Outline platelets.
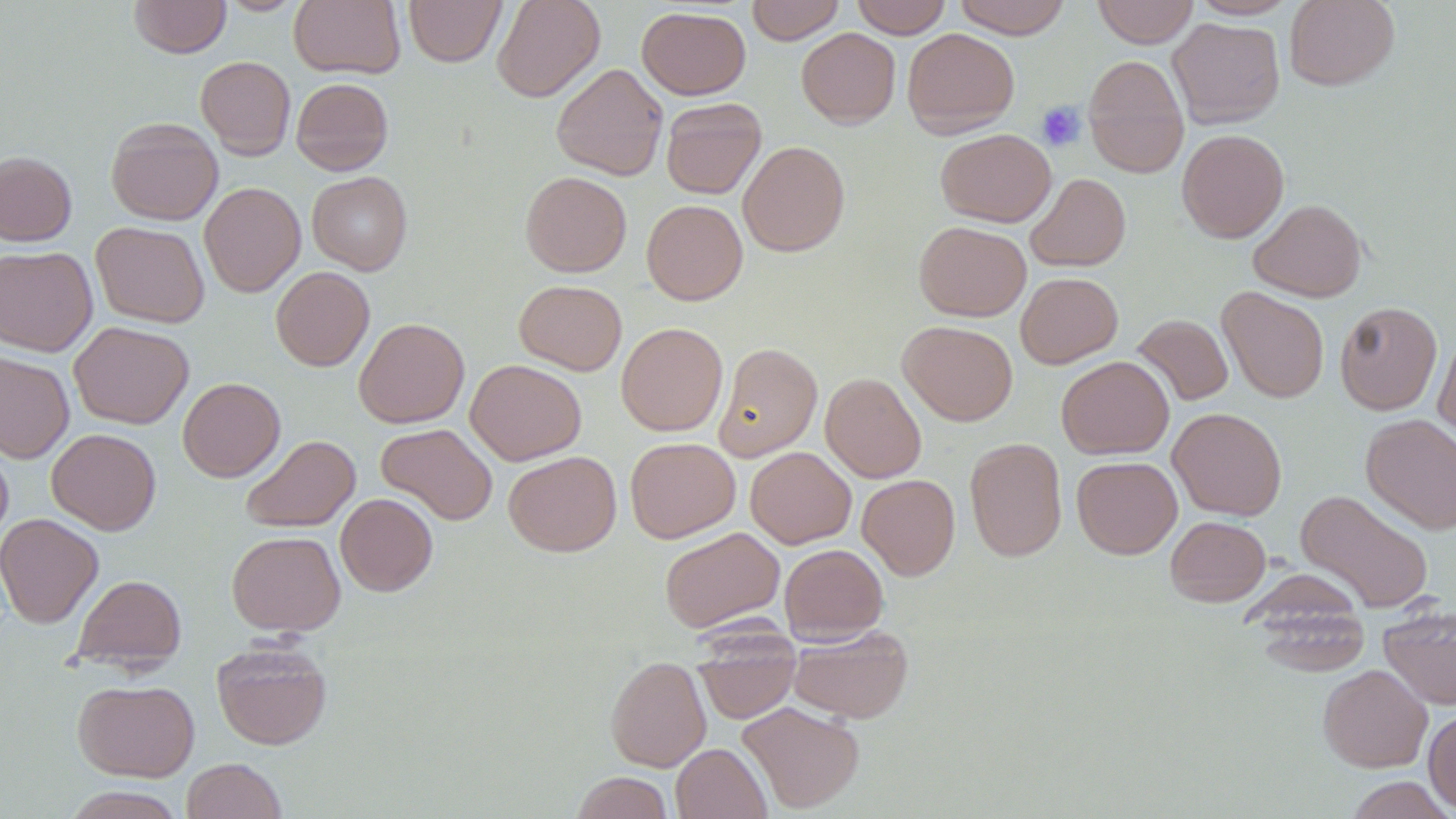
Approximate bounding boxes as named x1/y1/x2/y2 corners in pixels.
Platelets: (x1=1036, y1=101, x2=1086, y2=152).

slide-level diagnosis = no evidence of blood parasites
uninfected red blood cell locations = approximate bounding boxes as named x1/y1/x2/y2 corners in pixels: (x1=129, y1=0, x2=231, y2=57), (x1=289, y1=0, x2=405, y2=78), (x1=404, y1=0, x2=506, y2=67), (x1=492, y1=0, x2=605, y2=102), (x1=746, y1=0, x2=845, y2=44), (x1=850, y1=0, x2=952, y2=38), (x1=953, y1=0, x2=1072, y2=38), (x1=1092, y1=0, x2=1199, y2=48), (x1=1189, y1=0, x2=1297, y2=20), (x1=1284, y1=0, x2=1400, y2=90), (x1=637, y1=6, x2=751, y2=100), (x1=1168, y1=17, x2=1284, y2=128), (x1=797, y1=27, x2=901, y2=128), (x1=902, y1=28, x2=1020, y2=137), (x1=1083, y1=54, x2=1189, y2=178), (x1=195, y1=56, x2=296, y2=159), (x1=551, y1=63, x2=668, y2=180), (x1=291, y1=77, x2=394, y2=175), (x1=661, y1=97, x2=766, y2=200), (x1=106, y1=117, x2=223, y2=225), (x1=935, y1=128, x2=1056, y2=227), (x1=1177, y1=129, x2=1289, y2=243), (x1=738, y1=140, x2=850, y2=257), (x1=0, y1=150, x2=77, y2=246), (x1=307, y1=171, x2=412, y2=275), (x1=520, y1=171, x2=632, y2=277), (x1=1025, y1=173, x2=1131, y2=272), (x1=200, y1=182, x2=305, y2=297), (x1=1248, y1=198, x2=1367, y2=302), (x1=641, y1=199, x2=748, y2=305), (x1=91, y1=221, x2=210, y2=328), (x1=914, y1=221, x2=1031, y2=321), (x1=0, y1=246, x2=97, y2=356), (x1=271, y1=266, x2=375, y2=371), (x1=1016, y1=272, x2=1122, y2=369), (x1=514, y1=280, x2=627, y2=375), (x1=1217, y1=286, x2=1329, y2=403), (x1=1335, y1=301, x2=1442, y2=415), (x1=1132, y1=314, x2=1233, y2=406), (x1=354, y1=317, x2=470, y2=428), (x1=69, y1=321, x2=194, y2=429), (x1=898, y1=321, x2=1018, y2=426), (x1=616, y1=322, x2=729, y2=436), (x1=1432, y1=330, x2=1456, y2=450), (x1=714, y1=342, x2=823, y2=461), (x1=0, y1=352, x2=74, y2=462), (x1=1056, y1=356, x2=1174, y2=459), (x1=466, y1=360, x2=586, y2=465), (x1=820, y1=372, x2=926, y2=482), (x1=178, y1=377, x2=285, y2=482), (x1=1168, y1=407, x2=1286, y2=520), (x1=1361, y1=414, x2=1456, y2=534), (x1=375, y1=423, x2=498, y2=525), (x1=46, y1=429, x2=161, y2=535), (x1=242, y1=434, x2=360, y2=532), (x1=625, y1=437, x2=740, y2=543), (x1=965, y1=437, x2=1067, y2=562), (x1=0, y1=439, x2=13, y2=548), (x1=745, y1=446, x2=856, y2=548), (x1=503, y1=451, x2=621, y2=556), (x1=1071, y1=456, x2=1182, y2=558), (x1=857, y1=474, x2=960, y2=580), (x1=1295, y1=489, x2=1434, y2=613), (x1=335, y1=493, x2=438, y2=596), (x1=0, y1=513, x2=104, y2=629), (x1=1165, y1=515, x2=1270, y2=606), (x1=659, y1=527, x2=785, y2=633), (x1=226, y1=531, x2=345, y2=636), (x1=779, y1=543, x2=888, y2=644), (x1=73, y1=574, x2=187, y2=672), (x1=1245, y1=580, x2=1372, y2=676), (x1=1378, y1=606, x2=1456, y2=710), (x1=787, y1=625, x2=913, y2=724), (x1=693, y1=630, x2=801, y2=724), (x1=211, y1=640, x2=332, y2=750), (x1=605, y1=655, x2=711, y2=772), (x1=1318, y1=664, x2=1433, y2=772), (x1=73, y1=679, x2=200, y2=781), (x1=737, y1=701, x2=865, y2=814), (x1=1423, y1=708, x2=1456, y2=815), (x1=671, y1=743, x2=771, y2=819), (x1=181, y1=758, x2=287, y2=819), (x1=571, y1=772, x2=674, y2=819), (x1=1345, y1=776, x2=1453, y2=818), (x1=63, y1=786, x2=187, y2=818)
image size = 1456×819 pixels
preparation = thin blood film
field of view = single
stain = May-Grünwald-Giemsa
modality = light microscopy
magnification = 1000x